Assess this cell for malaria.
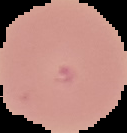
It is uninfected.

Summary:
  - Image type: segmented cell region with the area outside set to black
  - Preparation: thin blood film
  - Image size: 127×133 pixels